Comment on the morphology of the erythrocytes.
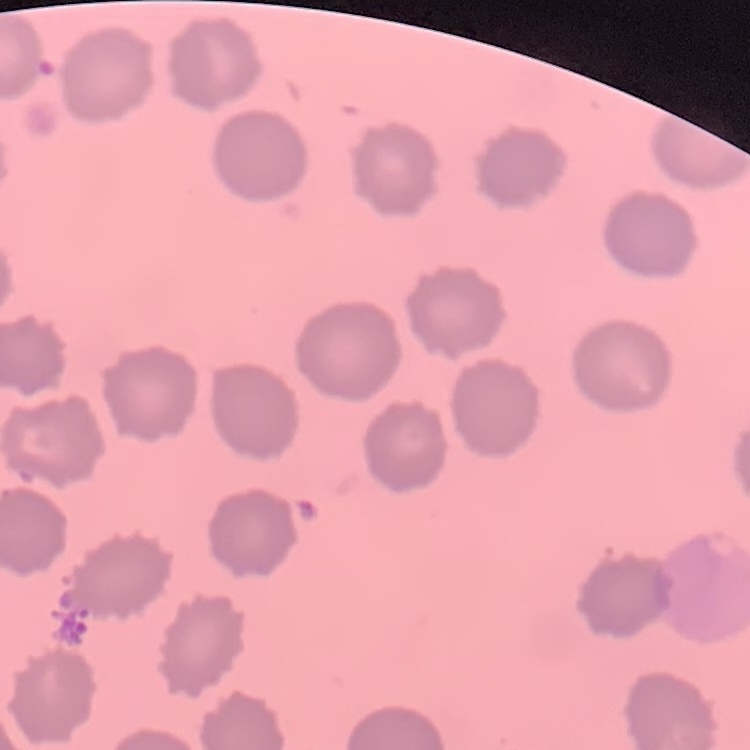
No rouleaux formation.

Field's or Giemsa stain. Square crop of a larger photomicrograph. Thin blood film.